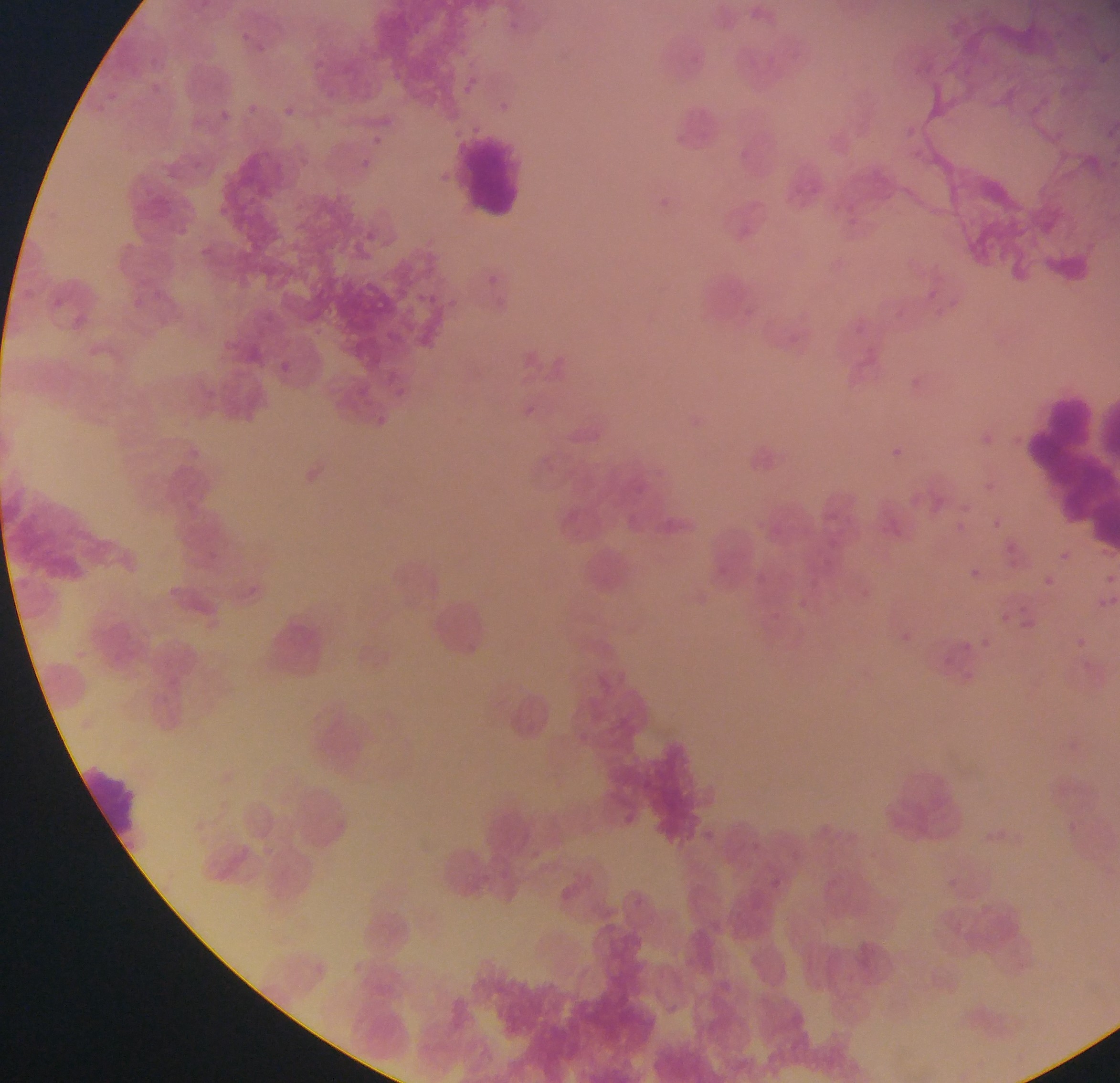

country = Ghana
image size = 1120×1083 pixels
field of view = single
malaria parasite locations = approximate bounding boxes as (left, top, right, bottom) in pixels: (240, 27, 254, 44), (313, 56, 326, 70), (457, 80, 472, 94), (102, 89, 118, 102), (498, 95, 510, 111), (241, 101, 256, 114), (283, 101, 301, 118), (221, 110, 234, 119), (906, 121, 921, 134), (369, 132, 385, 147), (356, 156, 374, 172), (435, 168, 449, 181), (656, 195, 675, 219), (370, 230, 383, 250), (488, 273, 501, 293), (928, 282, 937, 299), (419, 288, 441, 307), (952, 297, 960, 311), (932, 307, 941, 320), (271, 356, 297, 378), (901, 371, 926, 394), (525, 405, 541, 417), (981, 433, 995, 450), (882, 440, 910, 467), (985, 478, 994, 491), (961, 499, 972, 509), (989, 515, 1004, 530), (954, 518, 967, 533), (1003, 540, 1020, 559), (1055, 547, 1073, 563), (965, 564, 983, 582), (1102, 569, 1119, 585), (1040, 572, 1058, 589), (1094, 592, 1115, 612), (794, 594, 805, 607), (996, 608, 1018, 628), (893, 625, 918, 649), (1070, 632, 1095, 654), (979, 634, 995, 653), (958, 637, 975, 655), (619, 813, 639, 840), (701, 828, 716, 842), (528, 843, 542, 861), (761, 861, 773, 870), (493, 863, 507, 876), (768, 881, 781, 890), (560, 884, 575, 902)
capture = mobile-phone photograph through a microscope
leukocyte locations = approximate bounding boxes as (left, top, right, bottom) in pixels: (454, 133, 530, 218), (1030, 382, 1114, 502), (426, 594, 498, 666), (260, 613, 339, 688), (495, 684, 565, 752), (83, 763, 145, 850)
preparation = thin blood smear